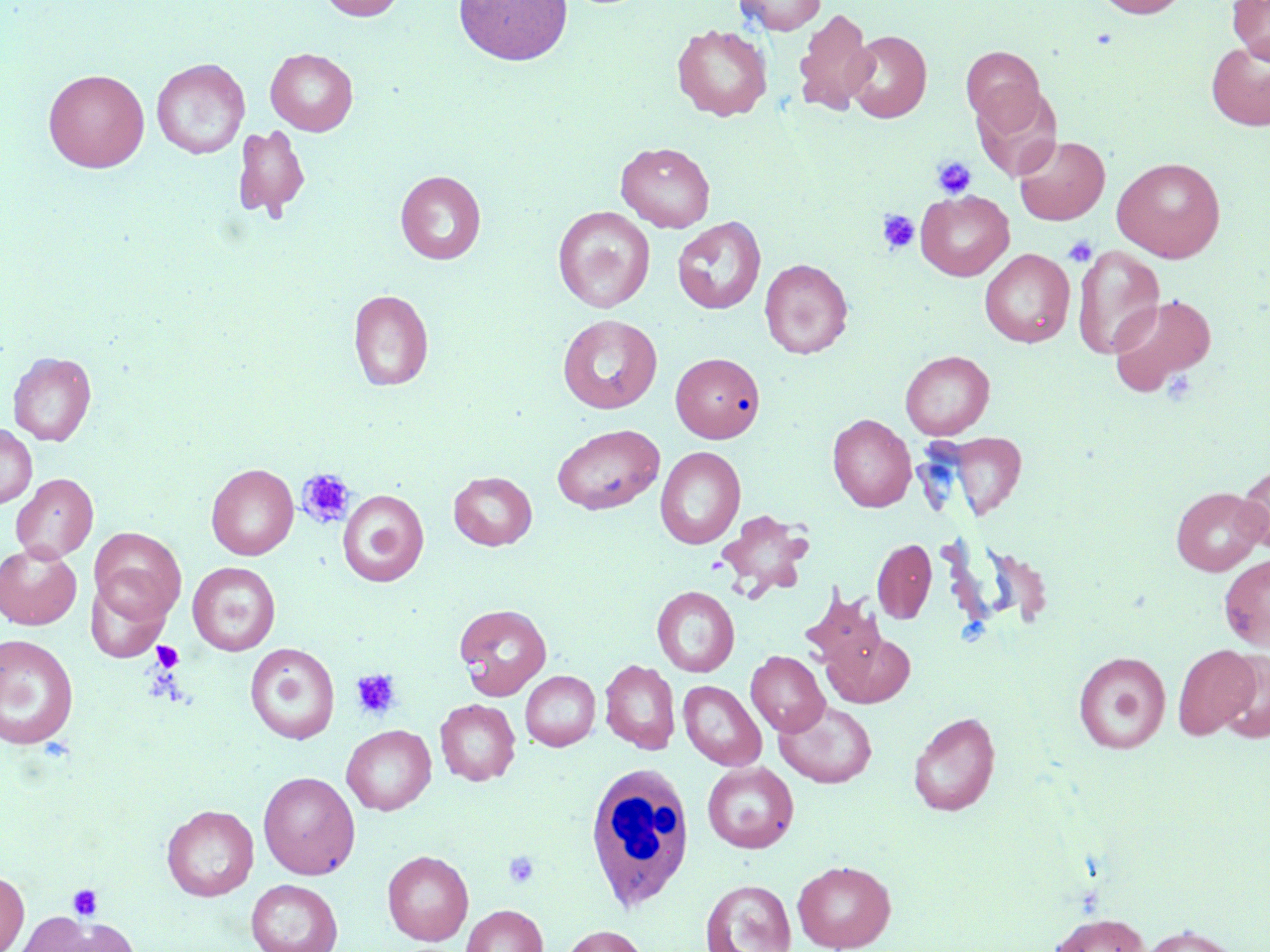
slide-level diagnosis = negative for blood parasites
modality = light microscopy
magnification = 1000x
stain = May-Grünwald-Giemsa
field of view = one of a larger specimen
white blood cell locations = approximate bounding boxes as named x1/y1/x2/y2 corners in pixels: (x1=589, y1=760, x2=695, y2=911)
uninfected red blood cell locations = approximate bounding boxes as named x1/y1/x2/y2 corners in pixels: (x1=317, y1=0, x2=406, y2=21), (x1=454, y1=0, x2=572, y2=65), (x1=733, y1=0, x2=826, y2=34), (x1=1095, y1=0, x2=1189, y2=18), (x1=1227, y1=0, x2=1270, y2=64), (x1=793, y1=8, x2=876, y2=116), (x1=672, y1=24, x2=772, y2=121), (x1=845, y1=31, x2=932, y2=122), (x1=1206, y1=41, x2=1270, y2=131), (x1=961, y1=46, x2=1046, y2=134), (x1=265, y1=48, x2=358, y2=136), (x1=151, y1=58, x2=249, y2=160), (x1=43, y1=68, x2=149, y2=173), (x1=972, y1=86, x2=1062, y2=182), (x1=232, y1=123, x2=311, y2=222), (x1=1013, y1=135, x2=1110, y2=225), (x1=616, y1=141, x2=715, y2=232), (x1=1112, y1=157, x2=1226, y2=262), (x1=395, y1=170, x2=486, y2=264), (x1=916, y1=190, x2=1014, y2=281), (x1=553, y1=206, x2=654, y2=313), (x1=672, y1=217, x2=766, y2=315), (x1=1073, y1=245, x2=1165, y2=359), (x1=979, y1=248, x2=1075, y2=348), (x1=760, y1=258, x2=852, y2=358), (x1=348, y1=289, x2=433, y2=392), (x1=1108, y1=293, x2=1217, y2=397), (x1=558, y1=314, x2=662, y2=413), (x1=900, y1=350, x2=994, y2=439), (x1=7, y1=351, x2=97, y2=446), (x1=673, y1=352, x2=765, y2=442), (x1=828, y1=413, x2=916, y2=511), (x1=0, y1=424, x2=37, y2=508), (x1=552, y1=424, x2=664, y2=515), (x1=940, y1=432, x2=1027, y2=519), (x1=655, y1=446, x2=745, y2=549), (x1=1237, y1=460, x2=1269, y2=555), (x1=206, y1=463, x2=299, y2=560), (x1=449, y1=471, x2=537, y2=550), (x1=11, y1=473, x2=98, y2=563), (x1=1170, y1=487, x2=1268, y2=575), (x1=338, y1=490, x2=428, y2=587), (x1=717, y1=509, x2=812, y2=599), (x1=89, y1=527, x2=186, y2=624), (x1=872, y1=538, x2=937, y2=623), (x1=0, y1=542, x2=82, y2=629), (x1=1219, y1=554, x2=1270, y2=651), (x1=188, y1=562, x2=280, y2=655), (x1=86, y1=579, x2=171, y2=660), (x1=652, y1=586, x2=739, y2=677), (x1=800, y1=588, x2=888, y2=675), (x1=454, y1=604, x2=552, y2=700), (x1=824, y1=630, x2=915, y2=708), (x1=0, y1=634, x2=79, y2=749), (x1=245, y1=643, x2=340, y2=744), (x1=1173, y1=644, x2=1259, y2=740), (x1=746, y1=651, x2=830, y2=736), (x1=1073, y1=651, x2=1171, y2=753), (x1=1217, y1=651, x2=1270, y2=743), (x1=599, y1=659, x2=680, y2=754), (x1=520, y1=671, x2=600, y2=751), (x1=678, y1=680, x2=766, y2=771), (x1=435, y1=699, x2=520, y2=786), (x1=775, y1=700, x2=876, y2=788), (x1=908, y1=712, x2=1000, y2=816), (x1=342, y1=725, x2=436, y2=815), (x1=703, y1=762, x2=799, y2=853), (x1=258, y1=771, x2=360, y2=879), (x1=162, y1=804, x2=258, y2=901), (x1=382, y1=850, x2=473, y2=945), (x1=793, y1=860, x2=896, y2=951), (x1=0, y1=869, x2=29, y2=952), (x1=246, y1=879, x2=343, y2=952), (x1=701, y1=879, x2=797, y2=952), (x1=461, y1=904, x2=548, y2=952), (x1=1048, y1=912, x2=1150, y2=952), (x1=17, y1=915, x2=136, y2=952), (x1=1138, y1=923, x2=1243, y2=952), (x1=558, y1=924, x2=650, y2=952)
platelet locations = approximate bounding boxes as named x1/y1/x2/y2 corners in pixels: (x1=932, y1=156, x2=976, y2=199), (x1=877, y1=209, x2=919, y2=254), (x1=1063, y1=236, x2=1098, y2=266), (x1=296, y1=468, x2=356, y2=528), (x1=151, y1=641, x2=184, y2=673), (x1=350, y1=669, x2=401, y2=720), (x1=503, y1=851, x2=540, y2=889), (x1=67, y1=883, x2=104, y2=920)
preparation = thin blood smear
image size = 1270×952 pixels